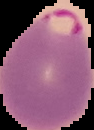

Summary:
  - Preparation: thin blood smear
  - Malaria status: parasitized
  - Image type: segmented cell region on a black background
  - Image size: 94×130 pixels